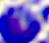 Micrograph. Captured at 400x magnification. A leukocyte is seen.